Name the blood parasite species.
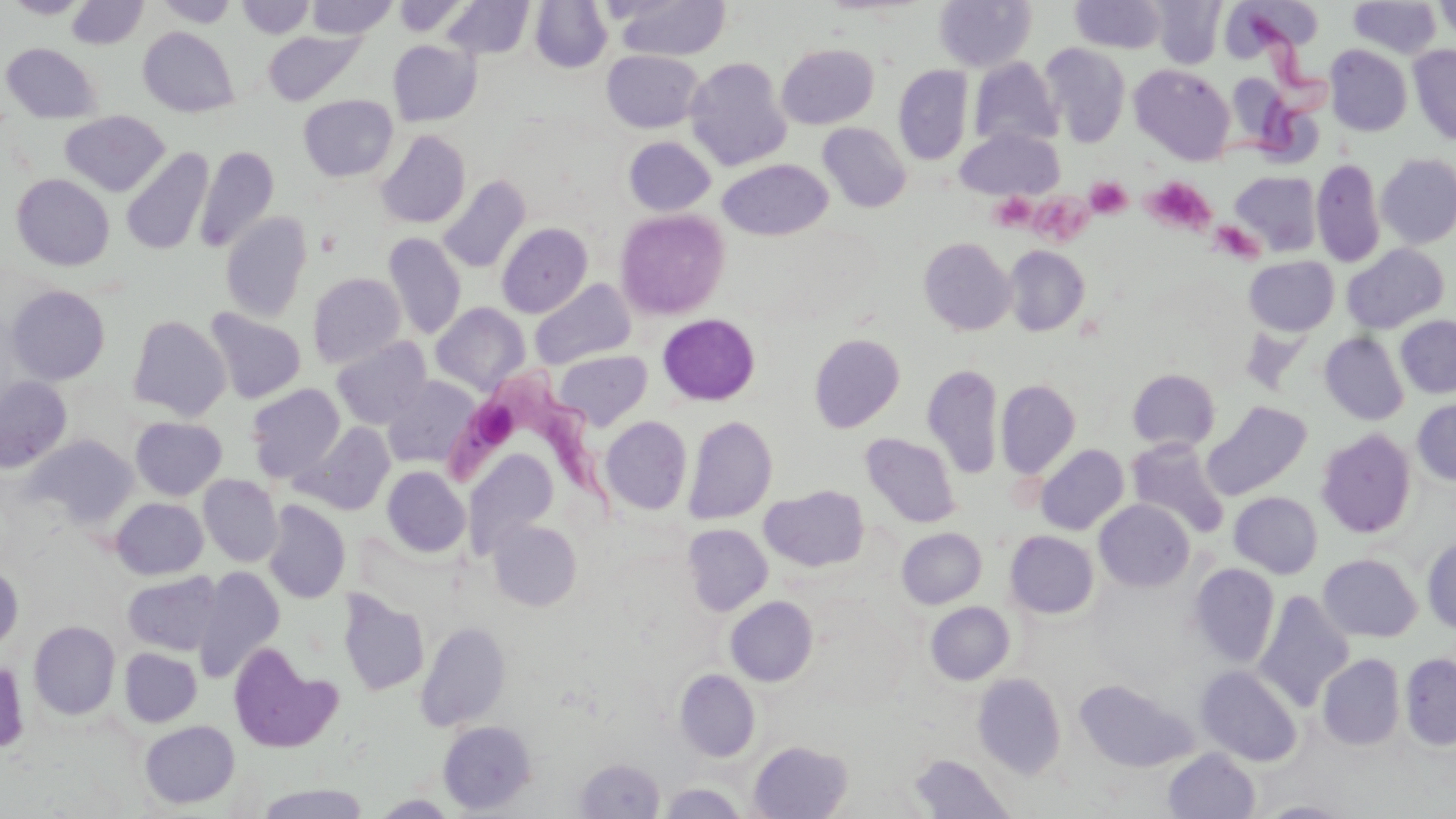
Trypanosoma brucei.

Approximate bounding boxes as [x1, y1, x2, y2] in pixels. Uninfected red blood cell locations: [5, 0, 89, 18], [155, 0, 239, 27], [237, 0, 315, 39], [306, 0, 397, 38], [392, 0, 470, 36], [441, 0, 534, 59], [612, 0, 732, 61], [934, 0, 1036, 73], [1152, 0, 1227, 68], [1232, 0, 1325, 53], [1434, 0, 1456, 43], [67, 1, 148, 49], [529, 1, 612, 73], [1070, 1, 1168, 53], [1348, 1, 1440, 59], [139, 27, 239, 118], [263, 30, 366, 106], [388, 40, 481, 126], [1040, 42, 1132, 147], [2, 43, 101, 123], [777, 43, 879, 129], [1325, 45, 1412, 136], [1409, 45, 1456, 145], [602, 50, 704, 132], [685, 57, 792, 171], [969, 57, 1063, 151], [1130, 64, 1236, 165], [893, 65, 973, 165], [1226, 74, 1292, 149], [298, 94, 398, 182], [60, 111, 170, 197], [818, 122, 912, 212], [955, 127, 1064, 199], [375, 129, 471, 228], [623, 136, 716, 216], [195, 145, 279, 254], [121, 146, 213, 256], [1375, 153, 1456, 249], [1311, 158, 1385, 268], [720, 160, 832, 241], [1230, 171, 1322, 256], [12, 174, 114, 271], [438, 175, 531, 273], [614, 209, 729, 320], [220, 212, 312, 322], [497, 223, 592, 317], [383, 232, 467, 340], [919, 237, 1016, 335], [1342, 243, 1450, 333], [1004, 245, 1090, 336], [1244, 256, 1339, 335], [307, 272, 406, 368], [529, 280, 635, 370], [7, 285, 110, 385], [431, 302, 531, 396], [204, 309, 306, 403], [657, 314, 760, 406], [127, 315, 231, 421], [1395, 315, 1456, 398], [1320, 332, 1409, 425], [810, 333, 904, 433], [331, 336, 432, 428], [554, 350, 652, 430], [922, 364, 1003, 479], [1127, 368, 1220, 452], [382, 375, 481, 469], [0, 376, 72, 473], [996, 379, 1080, 479], [246, 383, 345, 481], [1412, 398, 1456, 485], [1205, 401, 1312, 499], [601, 416, 692, 515], [683, 416, 777, 525], [130, 417, 227, 500], [294, 421, 396, 515], [1316, 428, 1416, 538], [860, 434, 961, 528], [25, 435, 138, 528], [1128, 438, 1229, 537], [1035, 444, 1129, 534], [461, 448, 560, 555], [382, 466, 470, 558], [199, 475, 282, 567], [760, 485, 869, 572], [1230, 492, 1323, 578], [111, 497, 208, 579], [1094, 499, 1194, 591], [263, 500, 351, 603], [488, 519, 582, 611], [682, 524, 772, 615], [897, 527, 986, 608], [1005, 530, 1099, 619], [1421, 536, 1456, 633], [1318, 554, 1421, 641], [0, 562, 23, 651], [1188, 563, 1279, 668], [193, 565, 284, 682], [123, 571, 222, 655], [337, 589, 429, 696], [1253, 590, 1355, 710], [725, 596, 818, 686], [926, 602, 1015, 684], [415, 620, 511, 731], [29, 621, 121, 720], [228, 642, 339, 752], [119, 647, 202, 727], [1400, 652, 1456, 749], [1317, 654, 1405, 750], [0, 658, 29, 753], [1197, 665, 1301, 767], [675, 669, 761, 762], [973, 673, 1066, 778], [1074, 680, 1193, 773], [139, 720, 239, 808], [438, 720, 537, 814], [748, 740, 853, 819], [1164, 748, 1260, 819], [909, 755, 1013, 818], [574, 758, 665, 818], [659, 782, 747, 819], [255, 783, 372, 818], [372, 794, 457, 818], [1258, 801, 1353, 818]. Platelet locations: [1142, 176, 1216, 235], [1086, 177, 1132, 219], [1036, 188, 1095, 249], [989, 193, 1035, 230], [1213, 220, 1268, 267]. Trypanosoma brucei locations: [445, 362, 610, 523]. May-Grünwald-Giemsa stain. One field of a larger specimen. Thin blood film. 1000x magnification. Optical microscopy. Image is 1456×819 pixels.